Assess the morphology of the red blood cells.
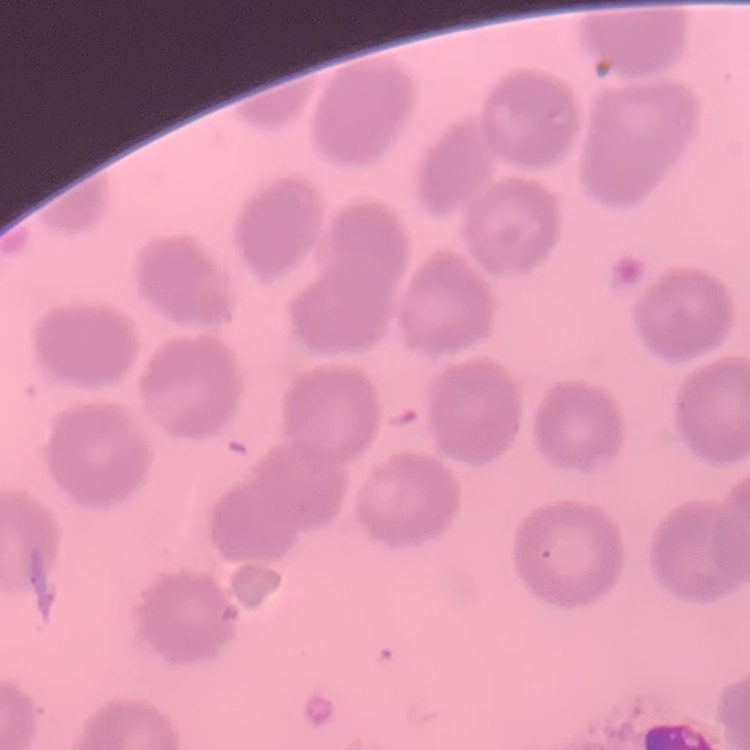

They show no rouleaux formation.

Summary:
  - Stain: Field's or Giemsa
  - Preparation: thin blood film
  - Image type: one tile cut from a larger photomicrograph